Classify this cell by malaria status.
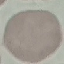
It is uninfected.

capture: smartphone through the microscope eyepiece
stain: Giemsa
preparation: thin blood film
image_type: cell patch, automatically extracted from a larger field of view and resized to 64 × 64 pixels